State which cell type is depicted.
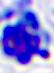
This is a leukocyte.

Captured at 400x magnification. Photomicrograph.